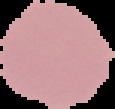

Image is 115×109 pixels. Malaria status: uninfected. Cell region segmented out of the field of view; the surrounding area is masked to black. From a thin blood film.